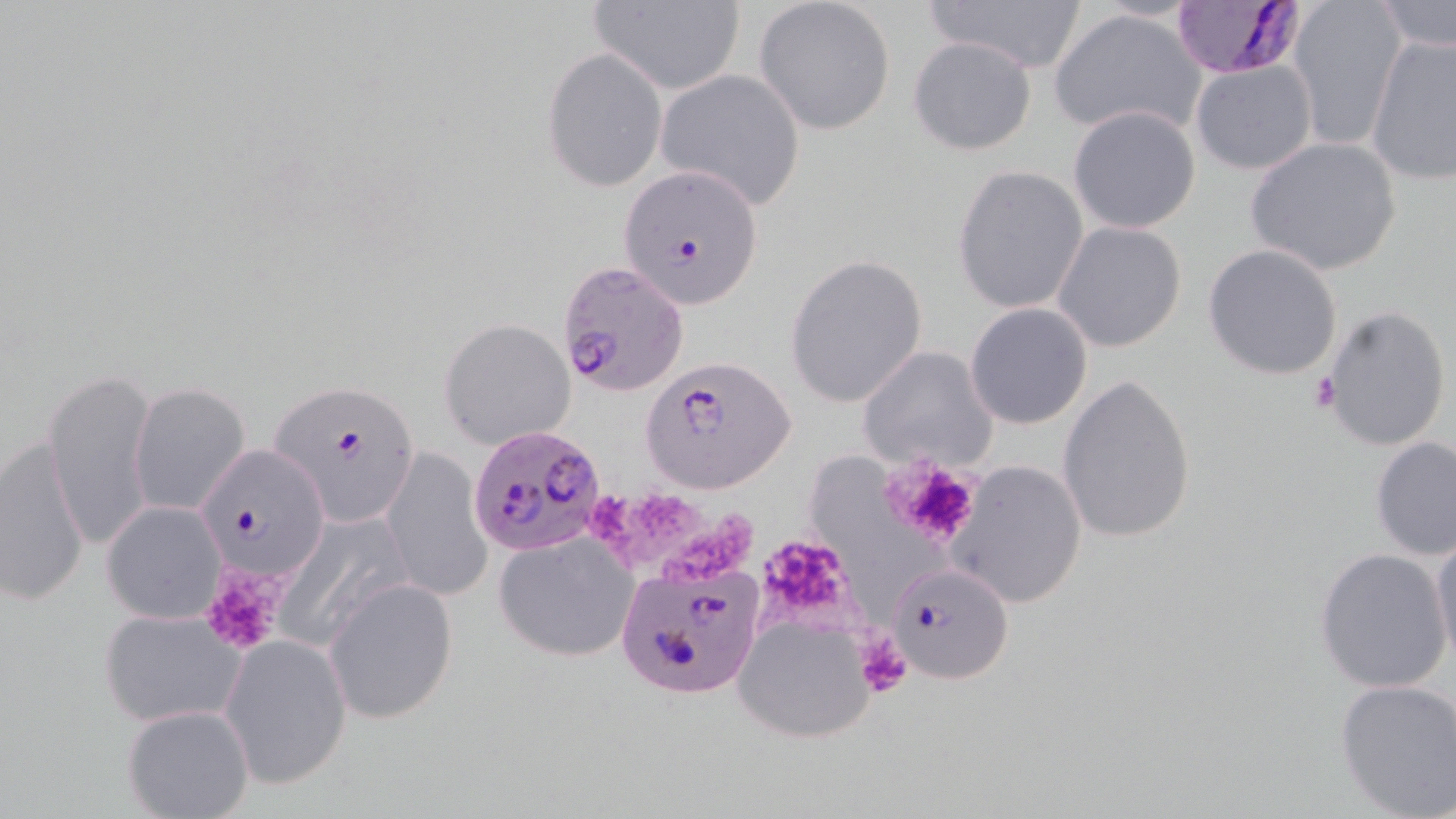

Approximate bounding boxes as (x1,y1)-(x2,y2) corner pairs in pixels. Platelet locations: (1310,371)-(1341,413), (885,457)-(980,551), (586,489)-(643,547), (630,492)-(701,570), (654,513)-(759,580), (757,531)-(858,631), (199,566)-(289,655), (856,632)-(914,699). Uninfected red blood cell locations: (754,0)-(896,134), (929,0)-(1086,76), (1287,0)-(1405,152), (1378,0)-(1456,55), (588,1)-(745,94), (1048,5)-(1209,138), (1365,33)-(1456,186), (907,35)-(1038,157), (543,46)-(668,192), (1190,60)-(1317,175), (656,69)-(807,209), (1067,106)-(1201,232), (1245,137)-(1401,274), (952,165)-(1089,315), (1053,222)-(1188,353), (1203,243)-(1343,380), (786,252)-(929,410), (964,303)-(1093,430), (1319,304)-(1451,453), (438,318)-(577,450), (857,346)-(999,471), (45,367)-(160,550), (1056,372)-(1198,544), (128,382)-(251,515), (1369,434)-(1456,560), (1,435)-(91,609), (381,448)-(493,602), (815,454)-(936,614), (948,458)-(1088,610), (101,500)-(227,624), (1428,529)-(1456,668), (494,533)-(638,662), (1314,547)-(1455,693), (326,579)-(457,723), (96,606)-(244,728), (733,610)-(877,746), (220,633)-(353,790), (1334,676)-(1456,818), (123,703)-(253,819). Plasmodium falciparum-infected red blood cell locations: (1174,1)-(1313,81), (618,163)-(764,307), (556,259)-(690,397), (640,357)-(799,495), (271,381)-(422,524), (468,425)-(607,556), (197,444)-(328,580), (614,554)-(762,701), (900,572)-(1014,684). Slide-level diagnosis: Plasmodium falciparum. May-Grünwald-Giemsa-stained preparation. 1000x magnification. Light microscopy. One field of a larger specimen. Thin blood film. Image is 1456×819 pixels.